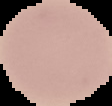 Image is 112×106 pixels. From a thin blood film. The area outside the segmented cell region is set to black. Result: no Plasmodium parasites seen.